Locate every leukocyte (white blood cell).
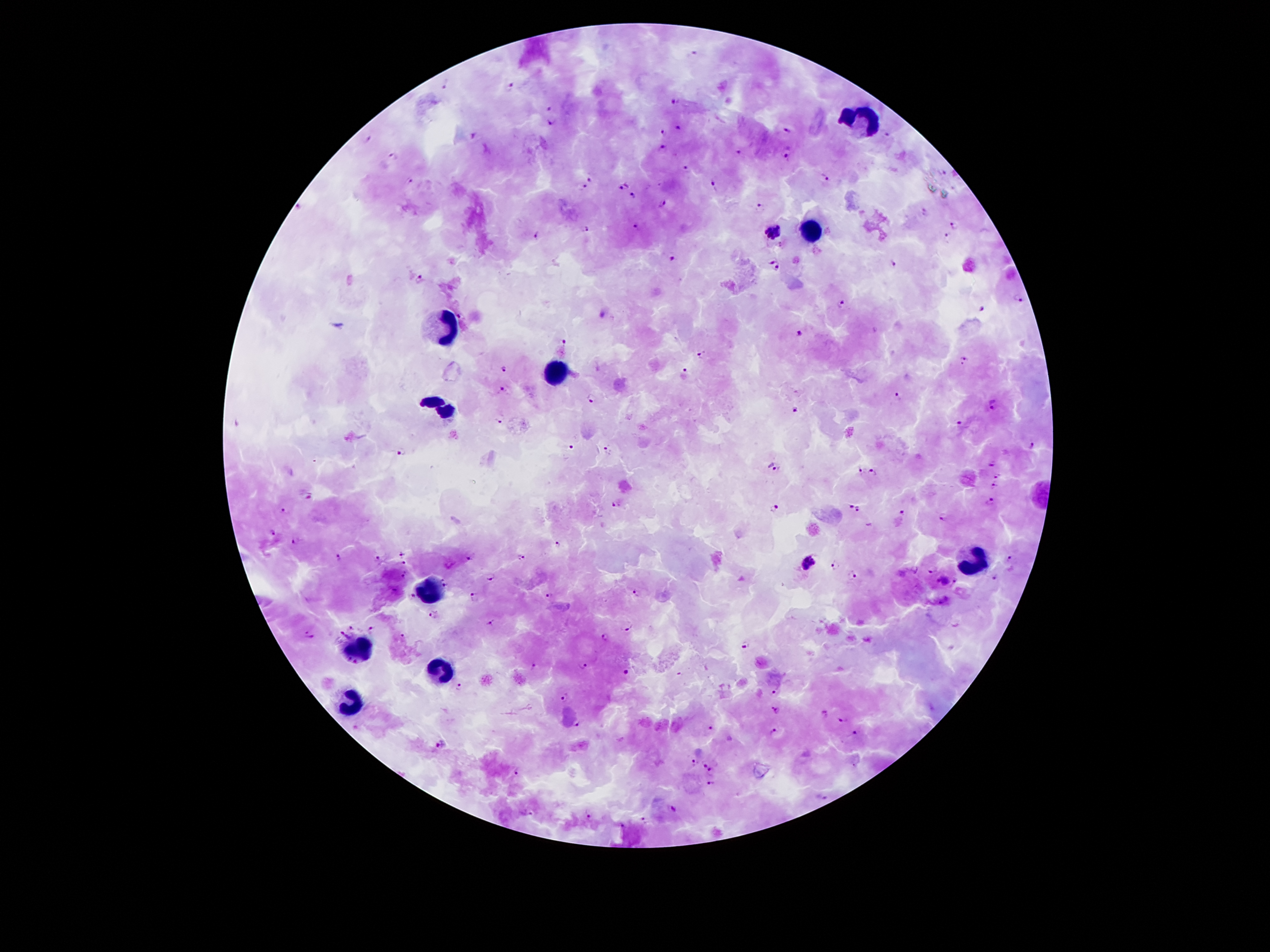

Approximate centers as {x, y} in pixels.
Leukocytes: {861, 119}, {812, 228}, {441, 329}, {556, 371}, {441, 405}, {972, 558}, {430, 589}, {356, 650}, {445, 665}, {350, 703}.

Summary:
  - Malaria parasite locations: {691, 53}, {444, 84}, {509, 87}, {676, 101}, {550, 106}, {551, 122}, {680, 125}, {787, 130}, {664, 131}, {887, 134}, {472, 136}, {367, 138}, {664, 147}, {738, 153}, {394, 155}, {786, 155}, {687, 170}, {591, 178}, {827, 178}, {412, 181}, {623, 186}, {714, 186}, {584, 187}, {633, 196}, {661, 204}, {298, 206}, {760, 207}, {925, 212}, {954, 225}, {638, 226}, {586, 231}, {775, 231}, {536, 235}, {947, 235}, {673, 258}, {771, 260}, {893, 265}, {780, 269}, {418, 279}, {1016, 300}, {843, 303}, {981, 307}, {602, 314}, {461, 316}, {799, 333}, {563, 342}, {703, 354}, {964, 361}, {504, 369}, {686, 369}, {501, 389}, {899, 396}, {590, 399}, {994, 404}, {794, 407}, {500, 417}, {959, 424}, {1033, 445}, {570, 448}, {401, 451}, {607, 451}, {992, 464}, {772, 466}, {860, 471}, {874, 471}, {999, 475}, {995, 485}, {310, 493}, {991, 500}, {617, 502}, {851, 505}, {776, 507}, {860, 509}, {284, 510}, {901, 513}, {944, 520}, {274, 533}, {295, 541}, {559, 545}, {402, 553}, {521, 555}, {340, 557}, {1010, 558}, {379, 559}, {470, 559}, {404, 563}, {807, 563}, {834, 566}, {931, 570}, {403, 573}, {993, 575}, {491, 577}, {854, 577}, {957, 580}, {942, 581}, {447, 584}, {636, 592}, {551, 594}, {412, 597}, {473, 597}, {944, 600}, {435, 615}, {491, 624}, {351, 627}, {372, 627}, {627, 629}, {343, 634}, {310, 635}, {403, 635}, {605, 637}, {746, 645}, {534, 664}, {583, 664}, {625, 671}, {459, 685}, {776, 693}, {564, 698}, {775, 711}, {824, 713}, {841, 720}, {577, 723}, {711, 726}, {773, 732}, {856, 732}, {442, 743}, {694, 760}, {704, 763}, {518, 770}, {712, 771}, {711, 784}, {821, 798}, {677, 808}, {530, 811}, {589, 814}, {644, 819}, {620, 825}
  - Patient malaria status: infected with Plasmodium falciparum
  - Magnification: 100x
  - Image size: 1270×952 pixels
  - Capture: smartphone camera through the microscope eyepiece
  - Preparation: thick peripheral-blood smear
  - Stain: Giemsa
  - Field of view: single